Name the parasite shown.
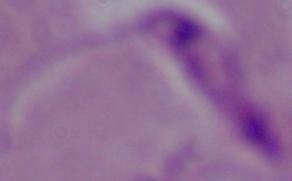

This is Leishmania.

Micrograph. Captured at 1000x magnification.